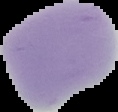
Summary:
  - Preparation: thin blood smear
  - Image type: cell region segmented out of the field of view; surrounding area masked to black
  - Result: negative for malaria parasites
  - Image size: 118×112 pixels